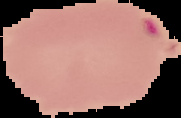

{
  "image_size": "181×118 pixels",
  "malaria_status": "parasitized",
  "preparation": "thin blood film",
  "image_type": "cell region segmented out of the field of view; surrounding area masked to black"
}